Describe the morphology of the erythrocytes.
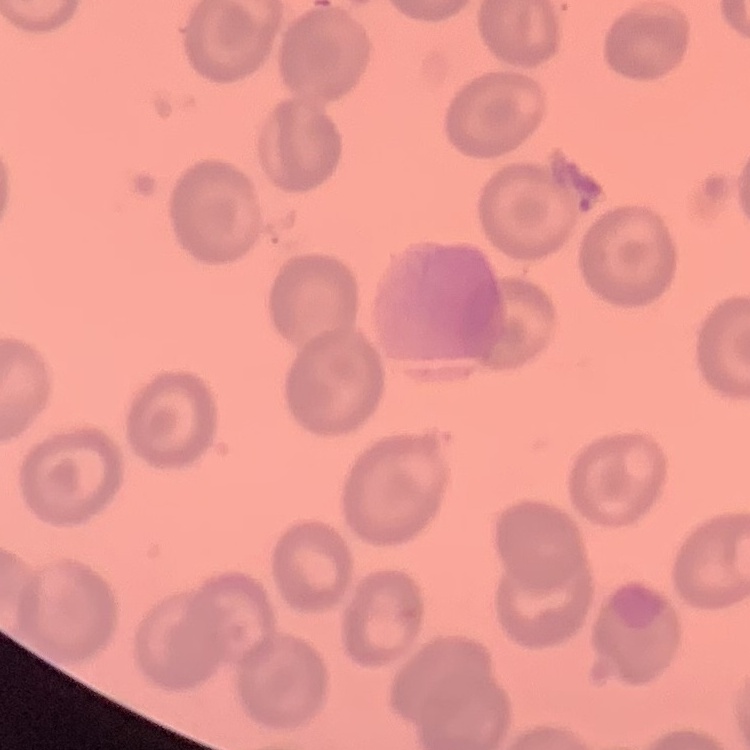
They show no rouleaux formation.

{
  "image_type": "one tile cut from a larger photomicrograph",
  "preparation": "thin peripheral smear",
  "stain": "Field's or Giemsa"
}